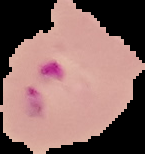

Summary:
  - Malaria status: parasitized
  - Preparation: thin blood smear
  - Image size: 145×154 pixels
  - Image type: cell region segmented out of the field of view; surrounding area masked to black